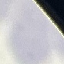
malaria status = uninfected
stain = Giemsa
capture = smartphone through the microscope eyepiece
preparation = thin smear
image type = cell patch, automatically extracted from a larger field of view and resized to 64 × 64 pixels